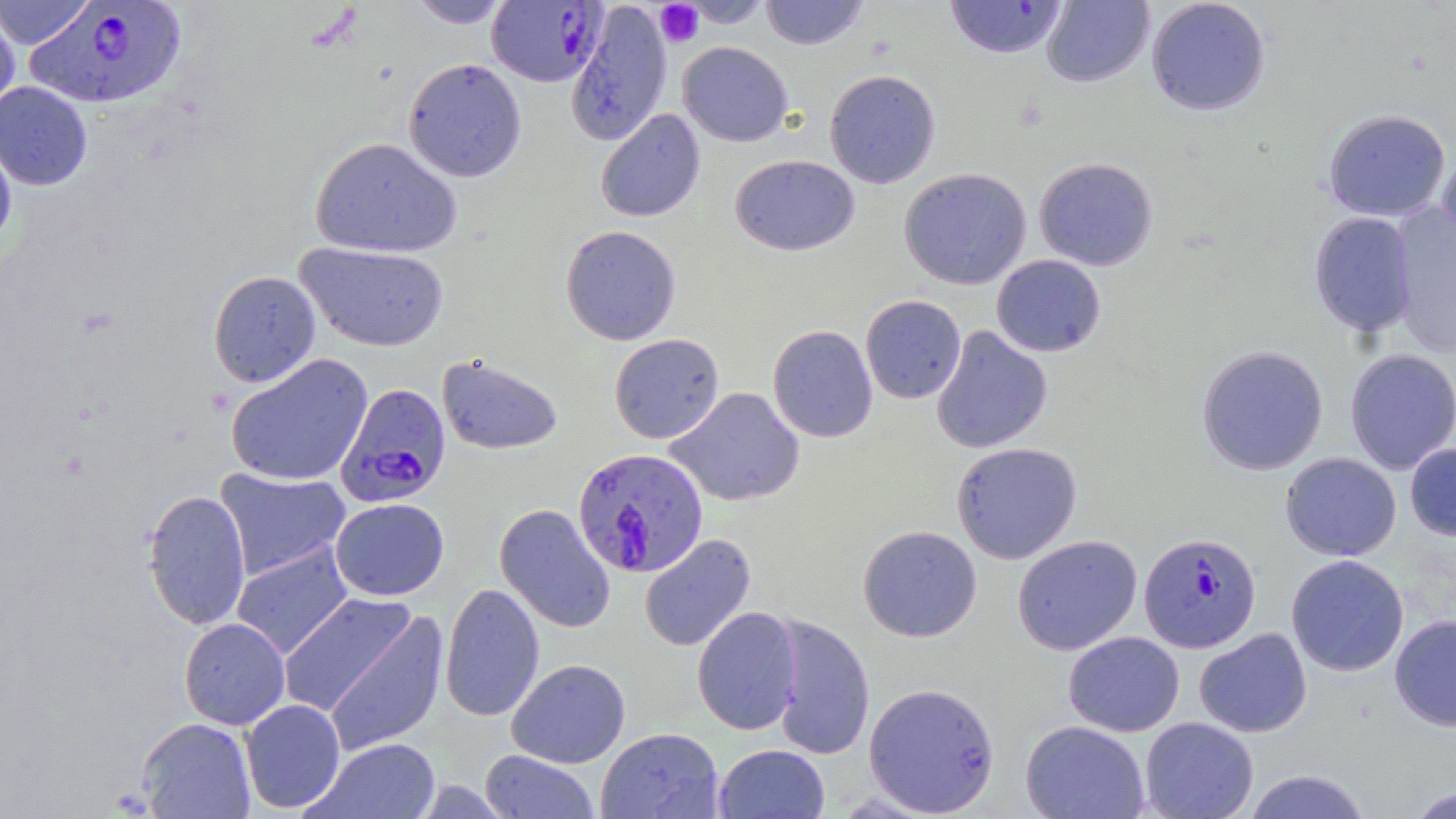 Approximate bounding boxes as (x1,y1)-(x2,y2) corner pairs in pixels. Plasmodium falciparum-infected red blood cell locations: (486,1)-(607,87), (24,2)-(188,109), (335,382)-(451,508), (572,448)-(708,577), (1138,532)-(1261,653). Platelet locations: (655,1)-(704,48). Uninfected red blood cell locations: (0,0)-(95,49), (408,0)-(513,28), (678,0)-(775,27), (759,0)-(869,50), (1041,0)-(1154,88), (1146,0)-(1270,116), (945,1)-(1068,59), (566,2)-(672,146), (0,9)-(20,118), (678,41)-(793,147), (403,58)-(526,182), (824,69)-(941,189), (0,82)-(92,190), (595,109)-(705,222), (1322,109)-(1450,221), (0,133)-(17,252), (310,137)-(461,258), (1437,146)-(1456,261), (730,154)-(859,256), (1034,157)-(1158,270), (899,167)-(1032,290), (1389,204)-(1456,356), (1309,211)-(1416,337), (560,225)-(681,345), (295,242)-(450,351), (991,254)-(1106,357), (208,270)-(321,387), (860,295)-(966,404), (767,325)-(878,442), (931,325)-(1053,454), (609,333)-(724,444), (1197,344)-(1328,476), (1344,348)-(1456,474), (225,353)-(373,487), (437,354)-(562,455), (666,387)-(805,507), (951,442)-(1082,564), (1405,443)-(1456,541), (1280,452)-(1402,561), (214,467)-(351,581), (142,489)-(251,630), (330,498)-(449,600), (495,504)-(616,633), (857,525)-(982,643), (639,533)-(756,652), (1012,535)-(1142,655), (231,543)-(354,659), (1286,554)-(1409,676), (440,582)-(544,722), (277,593)-(419,718), (692,606)-(803,735), (323,612)-(448,756), (768,614)-(876,760), (1389,614)-(1456,731), (179,618)-(290,730), (1194,628)-(1312,737), (1063,631)-(1184,737), (507,658)-(630,768), (863,681)-(1000,816), (240,699)-(346,813), (137,717)-(256,818), (1140,717)-(1258,819), (1021,720)-(1150,819), (596,727)-(724,819), (305,738)-(440,818), (714,743)-(830,818), (480,750)-(599,819), (1242,769)-(1372,818), (1405,786)-(1455,818). Slide-level diagnosis: Plasmodium falciparum. May-Grünwald-Giemsa-stained preparation. Optical microscopy. Image is 1456×819 pixels. One field of a larger specimen. 1000x magnification. Thin blood film.